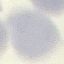

Summary:
  - Result: negative for malaria parasites
  - Capture: smartphone through the microscope eyepiece
  - Preparation: thin smear
  - Stain: Giemsa
  - Image type: cell patch, automatically extracted from a larger field of view and resized to 64 × 64 pixels